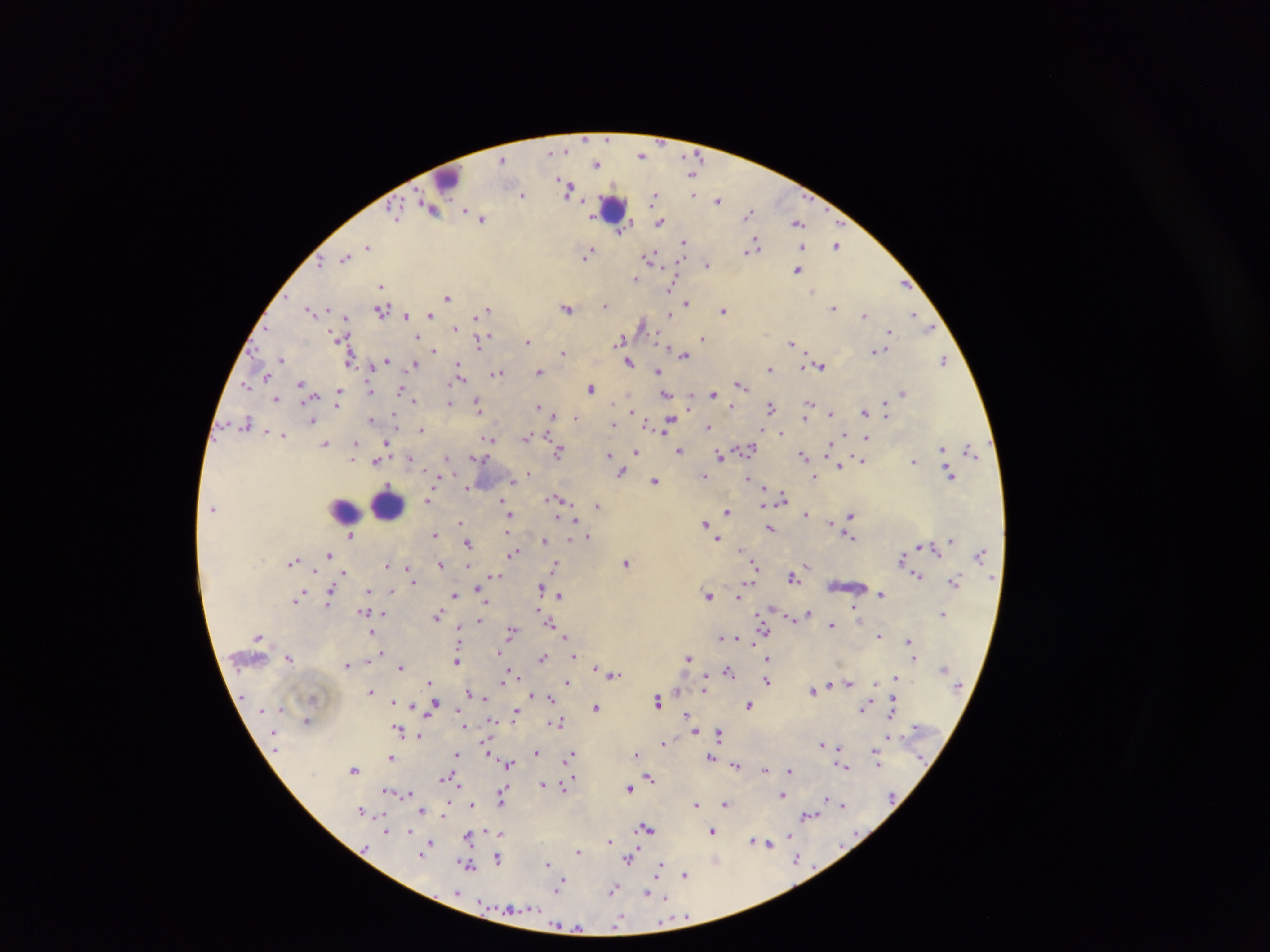 Approximate centers as (x, y) in pixels. Leukocyte locations: (447, 177), (613, 207), (388, 504), (344, 507). Malaria parasite locations: (641, 154), (503, 159), (596, 162), (569, 188), (522, 194), (694, 194), (655, 196), (718, 200), (431, 210), (394, 212), (748, 213), (482, 217), (660, 222), (799, 223), (621, 230), (684, 242), (838, 245), (753, 246), (368, 247), (804, 248), (589, 251), (586, 256), (345, 257), (651, 257), (320, 260), (708, 265), (798, 269), (636, 279), (904, 284), (381, 286), (671, 287), (814, 290), (448, 295), (687, 302), (606, 304), (568, 307), (833, 308), (311, 310), (488, 310), (724, 310), (381, 311), (671, 312), (864, 314), (914, 314), (406, 315), (430, 315), (345, 317), (642, 324), (455, 327), (930, 327), (889, 330), (337, 334), (418, 336), (702, 337), (340, 338), (621, 339), (480, 340), (528, 341), (791, 343), (433, 350), (877, 350), (563, 353), (684, 354), (281, 360), (351, 360), (944, 360), (386, 361), (629, 361), (414, 363), (458, 363), (822, 365), (770, 367), (804, 367), (539, 371), (658, 371), (498, 372), (267, 377), (462, 377), (301, 384), (741, 384), (245, 385), (591, 388), (402, 389), (370, 390), (339, 391), (713, 393), (902, 393), (405, 394), (666, 394), (276, 398), (690, 398), (414, 401), (450, 402), (689, 402), (810, 402), (477, 404), (732, 406), (538, 407), (771, 407), (632, 410), (865, 412), (394, 414), (831, 414), (886, 414), (553, 415), (575, 416), (806, 416), (371, 419), (312, 420), (670, 420), (246, 423), (613, 424), (708, 426), (421, 429), (662, 431), (781, 431), (268, 433), (282, 434), (843, 434), (527, 435), (867, 438), (490, 439), (326, 442), (387, 443), (828, 443), (356, 444), (748, 448), (943, 448), (970, 449), (680, 450), (559, 451), (635, 452), (355, 454), (609, 455), (447, 456), (475, 456), (720, 456), (803, 456), (410, 457), (612, 457), (354, 459), (862, 460), (376, 461), (914, 461), (840, 464), (426, 470), (528, 472), (622, 473), (949, 473), (703, 474), (814, 476), (749, 478), (512, 480), (655, 480), (466, 487), (764, 489), (782, 496), (557, 499), (428, 500), (502, 500), (765, 503), (597, 505), (504, 508), (727, 511), (806, 513), (510, 514), (851, 516), (574, 519), (832, 521), (460, 522), (705, 523), (770, 527), (508, 533), (434, 534), (352, 536), (850, 536), (588, 537), (718, 538), (545, 540), (950, 541), (468, 543), (919, 546), (741, 549), (514, 553), (330, 554), (901, 558), (294, 561), (626, 563), (754, 563), (387, 565), (441, 565), (556, 565), (408, 566), (467, 566), (807, 566), (345, 573), (496, 575), (918, 575), (793, 577), (953, 581), (414, 583), (746, 584), (541, 588), (370, 590), (392, 590), (331, 591), (881, 593), (302, 594), (454, 596), (559, 596), (709, 596), (739, 596), (297, 599), (328, 603), (853, 607), (538, 608), (365, 611), (808, 613), (383, 614), (761, 614), (943, 614), (790, 615), (803, 615), (438, 616), (479, 620), (550, 623), (832, 625), (459, 629), (764, 629), (371, 632), (511, 632), (878, 635), (259, 636), (566, 636), (720, 637), (737, 637), (910, 639), (752, 642), (498, 652), (382, 654), (576, 655), (689, 656), (542, 657), (768, 657), (289, 658), (914, 658), (370, 661), (456, 661), (346, 665), (400, 667), (596, 668), (729, 672), (509, 673), (616, 674), (894, 678), (706, 679), (767, 680), (503, 681), (431, 682), (568, 682), (849, 683), (829, 684), (875, 684), (370, 690), (813, 691), (704, 692), (471, 693), (672, 693), (678, 693), (531, 694), (552, 697), (487, 699), (658, 699), (393, 701), (411, 703), (395, 704), (749, 704), (434, 706), (455, 708), (596, 708), (865, 708), (892, 711), (515, 712), (429, 713), (688, 715), (491, 718), (307, 720), (557, 721), (463, 725), (398, 729), (696, 731), (719, 733), (419, 735), (888, 735), (488, 740), (664, 742), (822, 744), (487, 748), (875, 750), (536, 751), (571, 753), (637, 754), (456, 755), (711, 757), (391, 758), (509, 763), (736, 764), (878, 765), (843, 766), (766, 768), (354, 769), (790, 772), (573, 774), (650, 776), (444, 778), (571, 779), (456, 782), (543, 783), (563, 787), (504, 788), (629, 788), (387, 790), (409, 792), (784, 794), (502, 799), (829, 799), (447, 803), (838, 803), (696, 804), (726, 804), (843, 804), (471, 805), (445, 810), (362, 812), (422, 812), (809, 815), (647, 828), (487, 830), (713, 830), (386, 831), (410, 831), (496, 833), (502, 835), (789, 836), (469, 837), (753, 840), (609, 841), (759, 842), (430, 843), (767, 844), (578, 852), (421, 853), (796, 857), (498, 858), (628, 859), (715, 861), (661, 863), (549, 864), (469, 865), (659, 870), (685, 874), (559, 887), (614, 889), (648, 895), (665, 896), (684, 916), (618, 922). Image is 1270×952 pixels. Collected in Ghana. Single field of view. Thick blood smear. Photographed through a microscope with a mobile-phone camera.